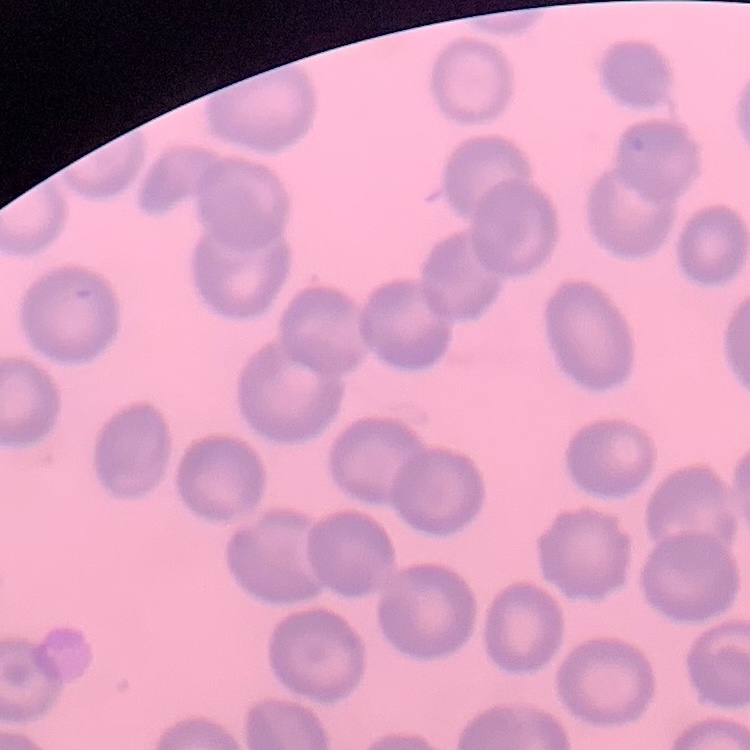
The erythrocytes exhibit no rouleaux formation. Thin blood film. Stained with either Field's or Giemsa. Square crop of a larger photomicrograph.